Identify the parasite.
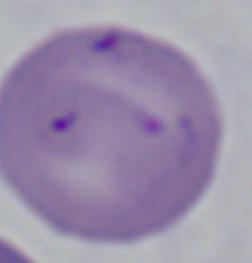
Babesia.

Micrograph. 1000x magnification.